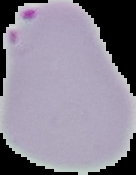 From a thin blood smear. Cell region segmented out of the field of view; the surrounding area is masked to black. Malaria status: parasitized. Image is 136×175 pixels.